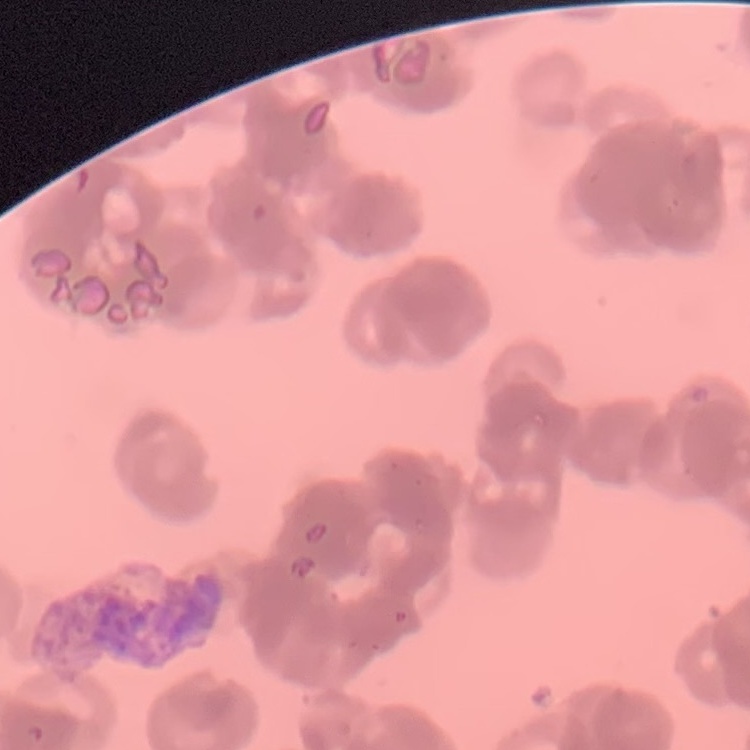

{
  "red_blood_cell_morphology": "rouleaux formation",
  "preparation": "thin peripheral smear",
  "stain": "Field's or Giemsa",
  "image_type": "one tile cut from a larger photomicrograph"
}